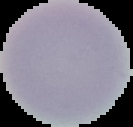

Summary:
  - Preparation: thin blood film
  - Malaria status: uninfected
  - Image type: cell region segmented out of the field of view; surrounding area masked to black
  - Image size: 133×127 pixels